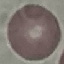

malaria status = uninfected
preparation = thin blood film
capture = smartphone camera at the microscope eyepiece
image type = automatically extracted cell patch, resized to 64 × 64 pixels
stain = Giemsa